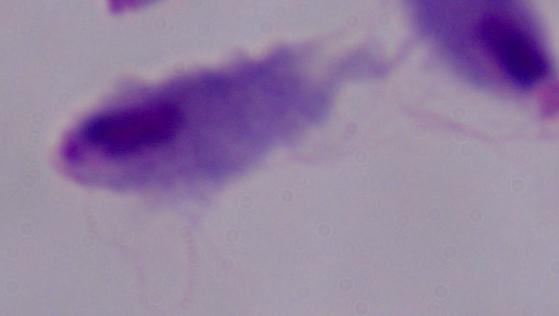
Summary:
  - Magnification: 1000x
  - Identification: trichomonad
  - Modality: photomicrograph